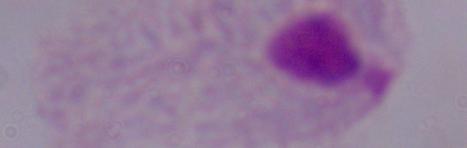

{
  "modality": "photomicrograph",
  "magnification": "1000x",
  "identification": "trichomonad"
}